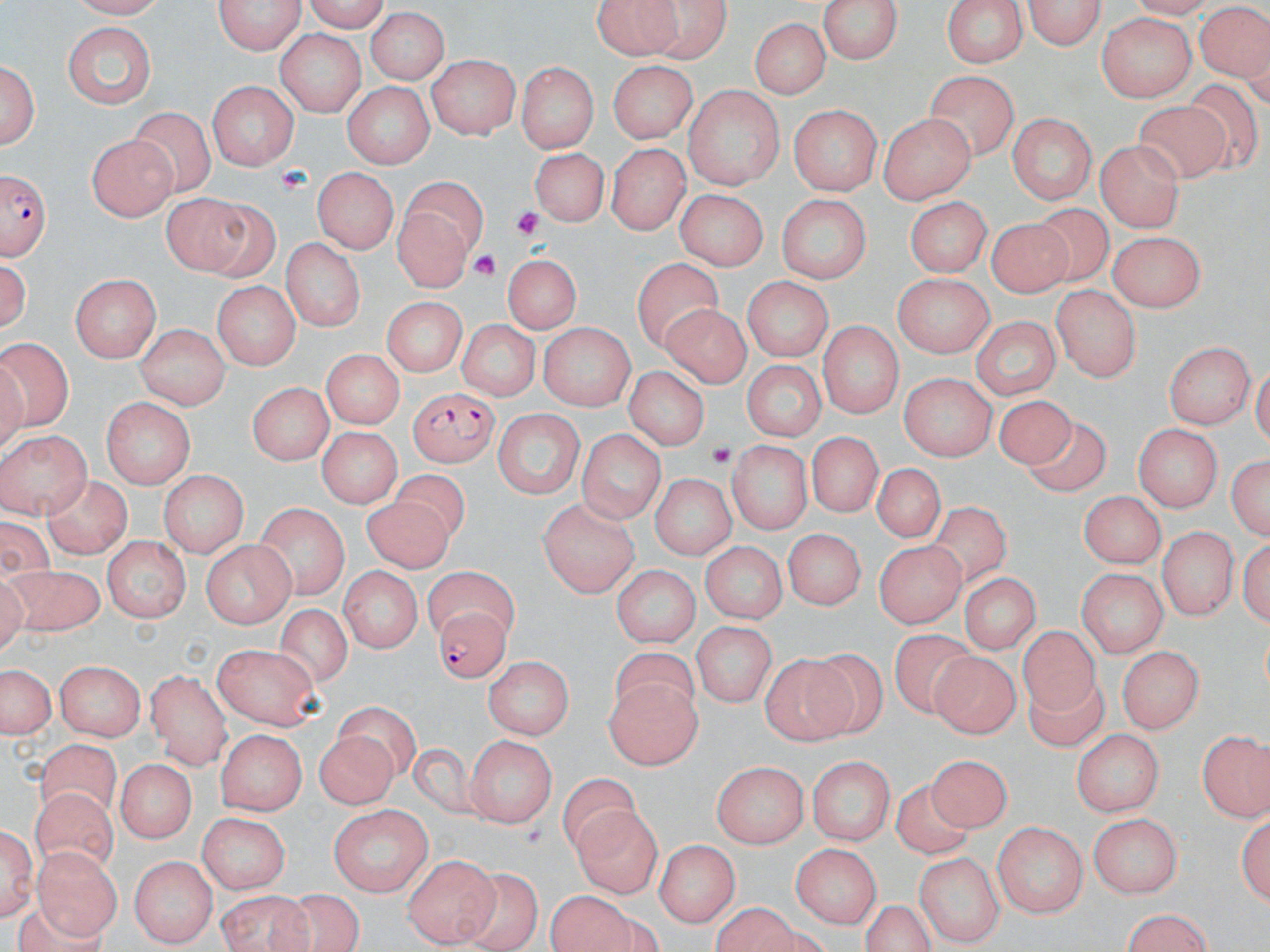
slide_level_diagnosis: Plasmodium falciparum
platelet_locations: 'approximate bounding boxes as [x1, y1, x2, y2] in pixels: [275, 163, 314, 192], [511, 206, 547, 241], [470, 251, 500, 281], [708, 437, 735, 472]'
preparation: thin blood smear
magnification: 1000x
modality: optical microscopy
plasmodium_falciparum_infected_red_blood_cell_locations: 'approximate bounding boxes as [x1, y1, x2, y2] in pixels: [0, 169, 48, 263], [410, 386, 497, 467], [433, 606, 510, 686]'
uninfected_red_blood_cell_locations: 'approximate bounding boxes as [x1, y1, x2, y2] in pixels: [68, 0, 168, 17], [212, 0, 307, 56], [817, 0, 907, 65], [941, 0, 1031, 69], [590, 2, 708, 60], [1022, 2, 1110, 47], [1196, 4, 1269, 88], [364, 10, 453, 84], [1097, 13, 1193, 103], [750, 17, 830, 99], [64, 22, 156, 110], [274, 28, 364, 115], [426, 58, 521, 140], [2, 59, 40, 154], [606, 61, 695, 145], [519, 65, 594, 152], [923, 72, 1019, 159], [208, 81, 301, 169], [340, 82, 436, 166], [685, 87, 783, 192], [1133, 101, 1226, 182], [788, 103, 879, 196], [133, 108, 214, 198], [880, 114, 975, 205], [1006, 115, 1098, 202], [86, 135, 180, 223], [1097, 141, 1186, 233], [529, 144, 612, 227], [608, 144, 688, 233], [311, 168, 396, 255], [398, 172, 489, 285], [674, 186, 764, 269], [774, 193, 877, 281], [162, 194, 268, 273], [903, 196, 994, 275], [1035, 203, 1114, 282], [992, 217, 1071, 300], [1108, 229, 1209, 314], [284, 238, 366, 333], [500, 254, 583, 335], [1, 255, 34, 336], [633, 257, 724, 351], [892, 272, 996, 354], [69, 273, 162, 360], [740, 275, 833, 360], [211, 281, 298, 370], [1052, 286, 1142, 383], [381, 299, 464, 380], [659, 300, 754, 391], [968, 315, 1059, 401], [454, 319, 539, 401], [817, 320, 904, 418], [540, 322, 635, 412], [133, 324, 231, 407], [0, 338, 76, 437], [1166, 339, 1254, 432], [323, 351, 400, 428], [739, 357, 829, 440], [619, 366, 711, 452], [899, 373, 995, 459], [247, 381, 330, 464], [100, 396, 197, 486], [993, 397, 1076, 473], [490, 409, 585, 501], [1027, 420, 1115, 502], [1132, 422, 1222, 513], [313, 426, 399, 510], [577, 427, 666, 525], [1, 429, 90, 517], [805, 433, 884, 515], [728, 439, 811, 539], [1229, 457, 1268, 542], [867, 464, 949, 545], [160, 469, 245, 557], [649, 471, 734, 560], [393, 472, 470, 547], [42, 476, 134, 560], [1079, 492, 1165, 571], [360, 494, 452, 574], [534, 496, 639, 599], [257, 505, 349, 604], [931, 505, 1014, 586], [785, 526, 868, 611], [1156, 529, 1236, 621], [101, 535, 188, 621], [197, 538, 296, 627], [704, 543, 783, 623], [876, 547, 969, 631], [4, 563, 109, 639], [342, 564, 421, 651], [610, 564, 700, 645], [965, 568, 1037, 656], [1079, 569, 1164, 661], [424, 570, 521, 640], [271, 604, 354, 691], [693, 618, 777, 705], [1018, 629, 1113, 718], [893, 632, 980, 719], [213, 644, 323, 733], [1115, 646, 1203, 736], [801, 649, 884, 734], [613, 650, 697, 720], [932, 650, 1017, 742], [483, 656, 574, 737], [753, 658, 865, 743], [56, 660, 146, 743], [0, 662, 55, 741], [145, 671, 233, 761], [1028, 678, 1106, 761], [605, 679, 700, 770], [335, 705, 415, 773], [1074, 727, 1163, 819], [218, 729, 305, 815], [312, 730, 395, 808], [1199, 730, 1268, 824], [466, 733, 555, 827], [35, 745, 120, 815], [409, 745, 475, 818], [806, 753, 894, 847], [932, 753, 1005, 831], [713, 760, 809, 846], [114, 761, 194, 843], [560, 775, 640, 859], [893, 783, 968, 859], [30, 787, 118, 873], [329, 805, 434, 898], [574, 807, 663, 897], [1237, 808, 1270, 911], [1090, 813, 1184, 898], [193, 814, 290, 894], [1, 819, 37, 922], [993, 820, 1087, 921], [657, 837, 742, 927], [790, 843, 880, 930], [32, 845, 120, 939], [915, 852, 1003, 946], [405, 853, 496, 947], [132, 855, 213, 947], [454, 870, 541, 951], [545, 888, 637, 951], [214, 893, 316, 952], [265, 893, 370, 952], [1118, 910, 1218, 951]'
image_size: 1270×952 pixels
stain: May-Grünwald-Giemsa
field_of_view: single